Classify this cell by malaria status.
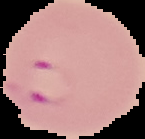
It is parasitized.

Segmented cell region on a black background. Image is 145×139 pixels. From a thin blood smear.